Locate every blood parasite and identify its species.
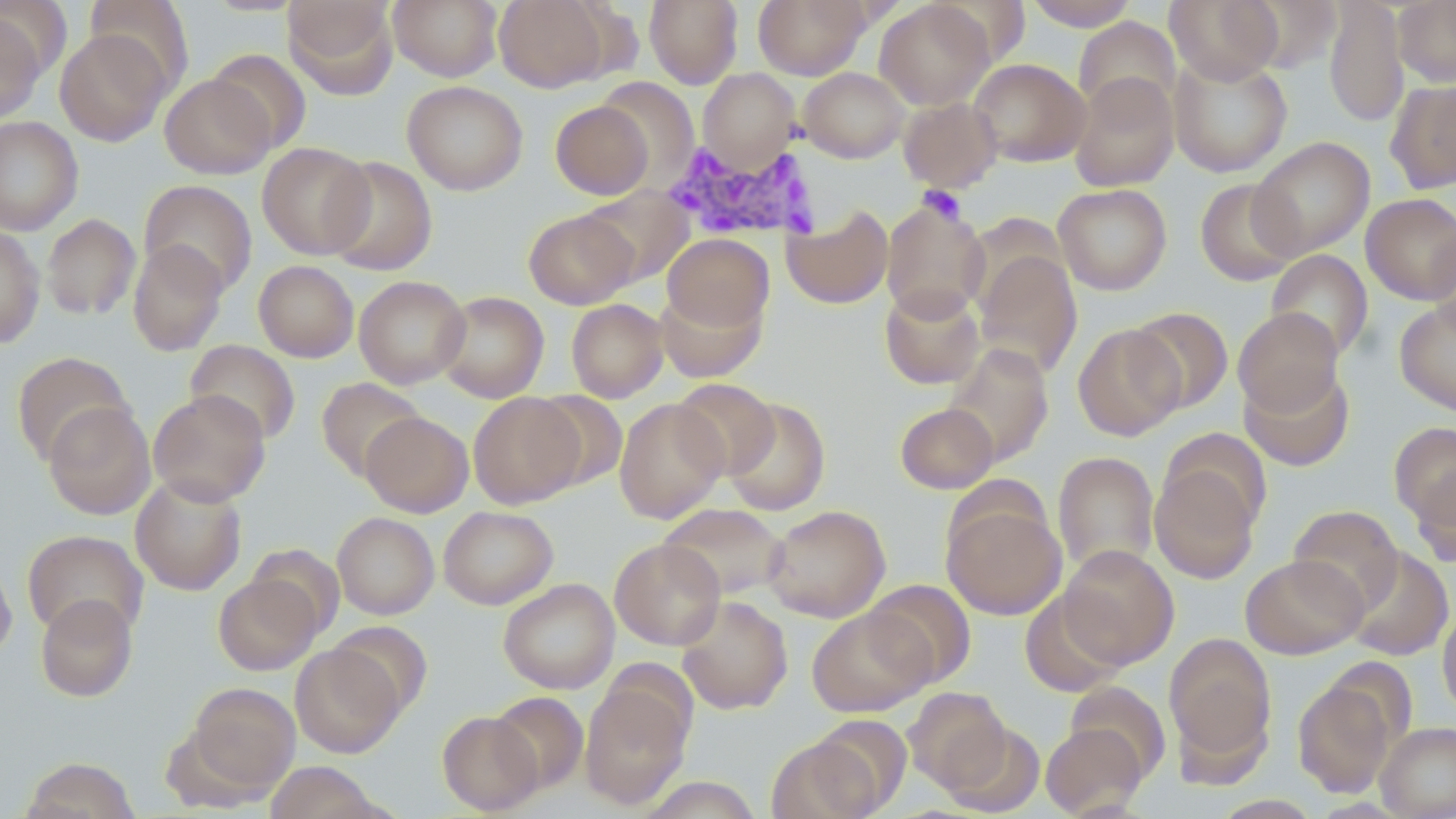

Approximate bounding boxes as (x1,y1)-(x2,y2) corner pairs in pixels.
Plasmodium malariae-infected red blood cells: (664,139)-(823,242).
No Plasmodium falciparum, Plasmodium ovale, Plasmodium vivax, Babesia divergens, or Trypanosoma brucei observed.

Summary:
  - Platelet locations: (918,186)-(966,225)
  - Uninfected red blood cell locations: (85,0)-(193,96), (283,0)-(398,97), (389,0)-(502,81), (495,0)-(612,91), (645,0)-(743,88), (753,0)-(870,79), (1023,0)-(1139,30), (1165,0)-(1284,85), (1324,0)-(1408,128), (1394,0)-(1456,87), (875,1)-(994,110), (0,11)-(46,125), (1073,17)-(1181,119), (55,29)-(171,146), (205,49)-(311,154), (1168,54)-(1293,177), (969,58)-(1091,167), (799,67)-(909,163), (697,68)-(801,169), (1068,72)-(1180,192), (160,73)-(276,178), (596,76)-(699,186), (1385,79)-(1456,194), (402,80)-(528,195), (898,96)-(1003,192), (550,100)-(654,200), (0,116)-(83,235), (1249,136)-(1375,258), (258,142)-(374,259), (323,156)-(437,276), (1194,178)-(1303,286), (139,179)-(258,295), (1053,183)-(1172,295), (577,186)-(693,286), (1361,193)-(1456,305), (880,197)-(991,322), (781,204)-(893,309), (523,208)-(638,309), (41,214)-(141,320), (0,225)-(46,349), (1427,227)-(1456,341), (662,233)-(774,333), (128,240)-(229,356), (974,249)-(1082,379), (1265,249)-(1373,362), (254,260)-(359,362), (354,275)-(470,389), (656,284)-(766,384), (879,285)-(985,389), (435,291)-(549,403), (566,298)-(668,402), (1395,298)-(1456,416), (1128,306)-(1234,414), (1233,307)-(1344,416), (1072,323)-(1186,441), (185,339)-(301,445), (943,343)-(1053,466), (12,351)-(133,465), (1240,364)-(1354,471), (316,376)-(427,481), (671,378)-(780,480), (148,389)-(270,506), (531,391)-(627,490), (468,392)-(585,508), (722,397)-(831,516), (613,398)-(728,524), (43,401)-(156,520), (894,402)-(999,494), (360,411)-(474,516), (1388,421)-(1456,529), (1158,430)-(1269,535), (1053,451)-(1159,576), (1149,461)-(1261,584), (1411,463)-(1456,568), (131,474)-(247,595), (942,497)-(1067,620), (658,502)-(789,600), (763,504)-(890,623), (439,505)-(558,610), (1287,505)-(1404,612), (332,512)-(439,619), (22,529)-(149,639), (610,538)-(725,649), (247,543)-(345,638), (1058,544)-(1179,669), (1343,546)-(1454,661), (1241,553)-(1368,659), (0,559)-(17,659), (213,574)-(322,675), (498,578)-(620,694), (865,579)-(976,689), (1020,590)-(1129,696), (36,593)-(137,701), (676,595)-(793,714), (1437,605)-(1456,719), (807,606)-(933,716), (328,621)-(433,717), (1164,632)-(1276,768), (290,643)-(404,757), (1292,676)-(1399,798), (579,677)-(693,809), (1065,681)-(1170,783), (184,682)-(300,796), (903,686)-(1011,792), (489,691)-(589,793), (437,711)-(543,815), (941,721)-(1045,816), (1376,721)-(1456,819), (1040,722)-(1147,818), (767,733)-(880,819), (21,757)-(140,818), (265,761)-(382,818), (637,776)-(765,817)
  - Slide-level diagnosis: Plasmodium malariae
  - Field of view: single
  - Modality: optical microscopy
  - Image size: 1456×819 pixels
  - Magnification: 1000x
  - Stain: May-Grünwald-Giemsa
  - Preparation: thin blood film